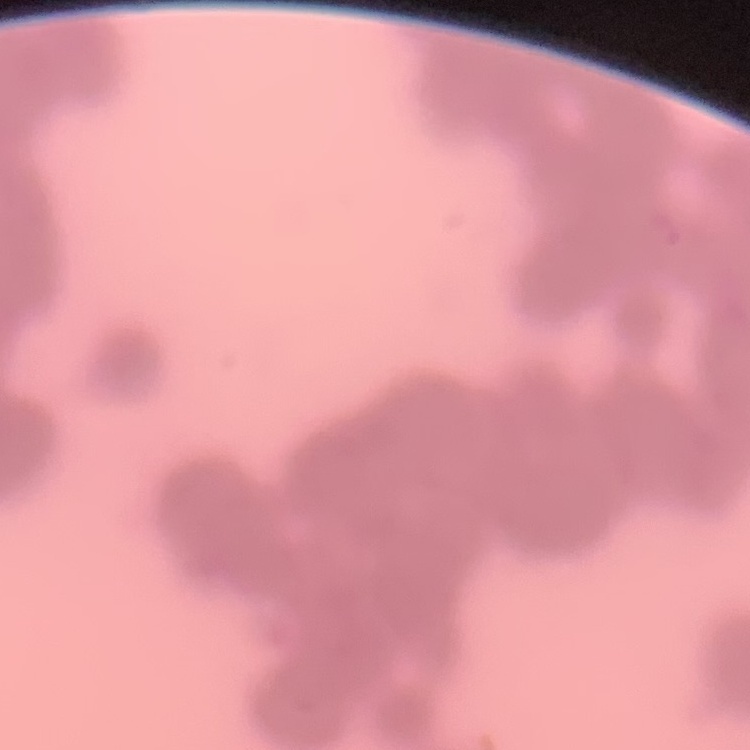

{
  "red_blood_cell_morphology": "rouleaux formation",
  "preparation": "thin blood film",
  "image_type": "one tile cut from a larger photomicrograph",
  "stain": "Field's or Giemsa"
}